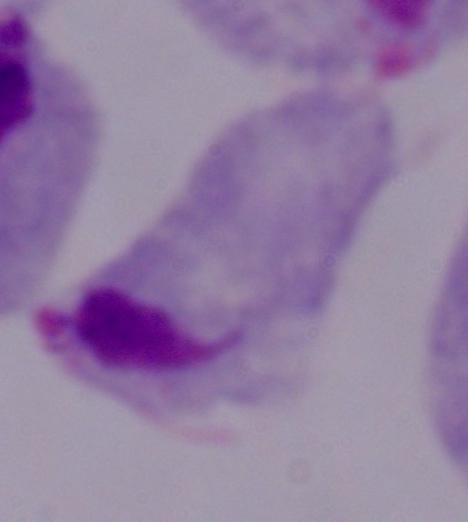

1000x magnification. Photomicrograph. A trichomonad is shown.